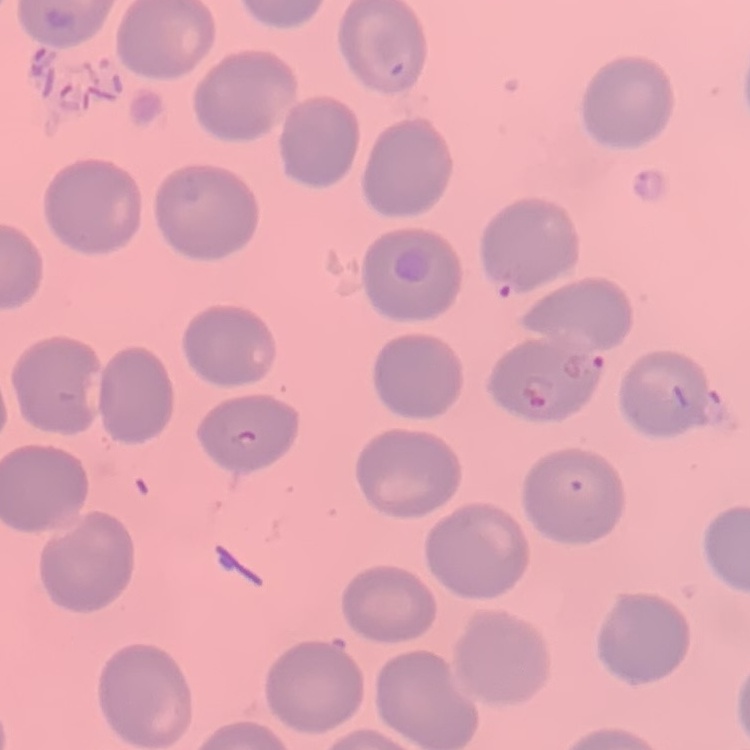
{
  "erythrocyte_morphology": "no rouleaux formation",
  "preparation": "thin peripheral smear",
  "image_type": "square crop of a larger photomicrograph",
  "stain": "Field's or Giemsa"
}